Name the blood parasite species.
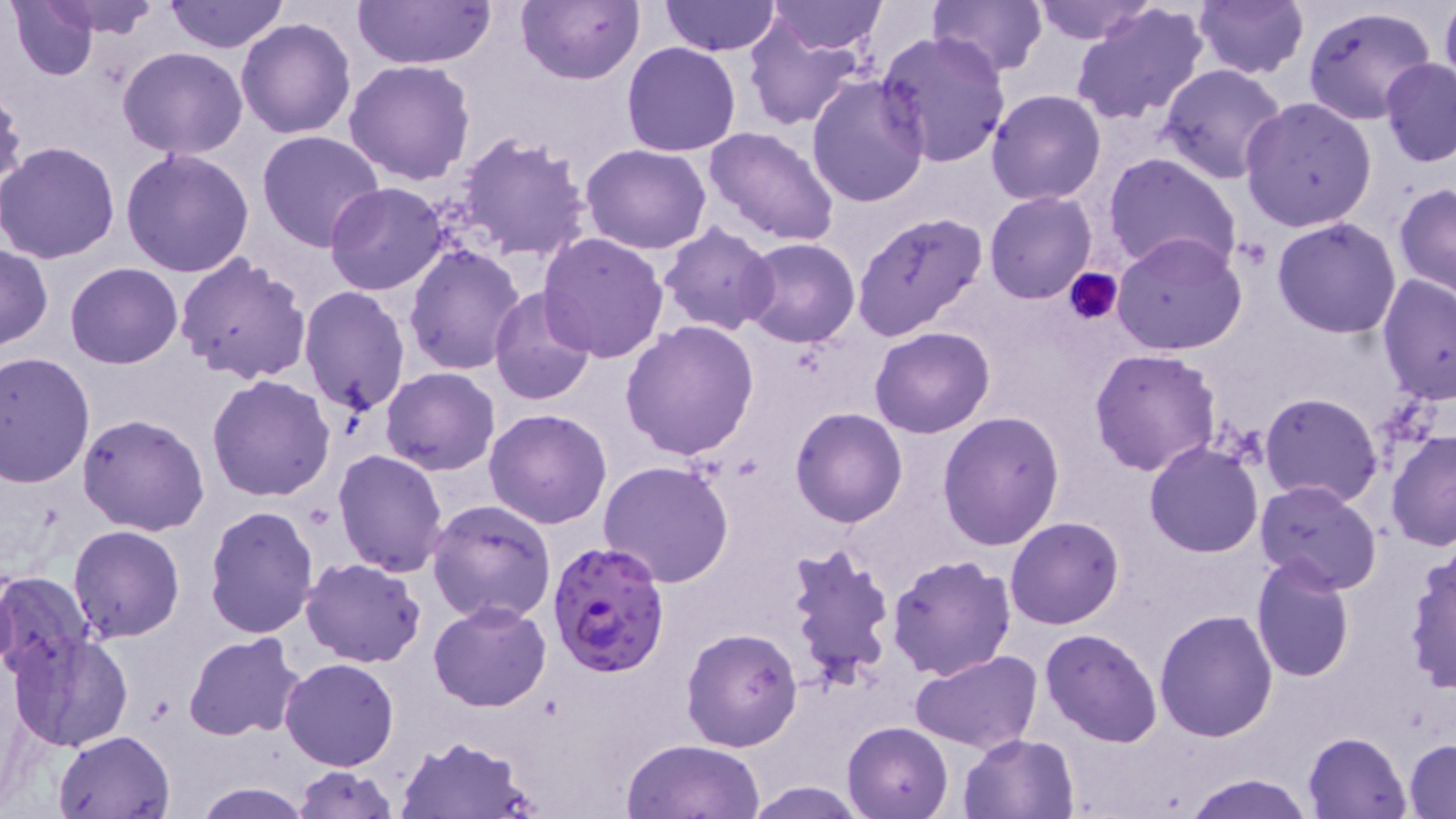
Plasmodium falciparum.

Approximate bounding boxes as (x1,y1)-(x2,y2) corner pairs in pixels. Uninfected red blood cell locations: (7,0)-(100,81), (33,0)-(168,38), (164,0)-(288,53), (354,0)-(496,71), (516,0)-(642,85), (659,0)-(782,57), (928,0)-(1047,77), (1029,0)-(1159,45), (1192,0)-(1310,78), (1440,0)-(1456,97), (767,1)-(888,52), (1070,1)-(1212,127), (1302,6)-(1437,127), (742,15)-(866,131), (237,18)-(357,138), (876,31)-(1011,167), (622,41)-(742,157), (117,46)-(249,160), (1379,56)-(1456,166), (344,60)-(476,187), (1158,62)-(1290,184), (806,75)-(930,209), (0,85)-(27,209), (987,89)-(1106,205), (1239,96)-(1377,233), (702,125)-(841,247), (256,129)-(385,252), (455,132)-(592,265), (0,141)-(122,263), (580,143)-(713,253), (121,150)-(255,280), (1102,152)-(1242,277), (325,183)-(450,295), (1394,183)-(1456,298), (983,191)-(1097,304), (851,211)-(988,343), (1272,217)-(1402,338), (658,223)-(779,334), (538,232)-(669,362), (1110,232)-(1248,355), (739,238)-(860,350), (0,243)-(52,350), (404,243)-(529,376), (173,254)-(311,386), (65,262)-(184,368), (1378,274)-(1455,405), (299,285)-(412,415), (487,287)-(597,405), (620,321)-(761,460), (870,327)-(996,439), (1089,349)-(1222,477), (0,351)-(96,487), (380,368)-(501,475), (207,374)-(336,501), (1259,392)-(1383,508), (485,408)-(613,529), (790,408)-(908,527), (937,411)-(1065,550), (77,413)-(210,535), (1386,430)-(1456,551), (1144,441)-(1264,557), (333,448)-(450,578), (597,460)-(735,588), (1255,481)-(1384,597), (426,498)-(558,626), (204,503)-(319,639), (1005,517)-(1124,630), (69,526)-(184,643), (783,539)-(897,689), (1403,544)-(1456,694), (887,554)-(1018,681), (1249,554)-(1357,683), (300,558)-(426,668), (0,571)-(97,680), (429,601)-(552,713), (1154,608)-(1278,742), (681,627)-(802,753), (1041,628)-(1162,748), (9,631)-(135,753), (184,633)-(308,742), (911,651)-(1041,752), (280,657)-(400,771), (843,721)-(952,818), (54,729)-(176,819), (1303,731)-(1412,818), (959,732)-(1080,819), (394,735)-(538,818), (622,738)-(766,819), (1406,739)-(1456,816), (291,765)-(398,819), (1186,773)-(1313,818), (740,780)-(871,818), (191,781)-(315,818). Platelet locations: (1066,265)-(1122,323). Plasmodium falciparum-infected red blood cell locations: (546,540)-(670,680). Single field of view. Thin blood smear. May-Grünwald-Giemsa stain. Image is 1456×819 pixels. Light microscopy. 1000x magnification.